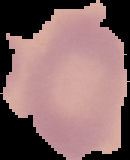 Image is 130×160 pixels. Malaria status: uninfected. From a thin blood smear. The area outside the segmented cell region is set to black.